Locate every Plasmodium parasite.
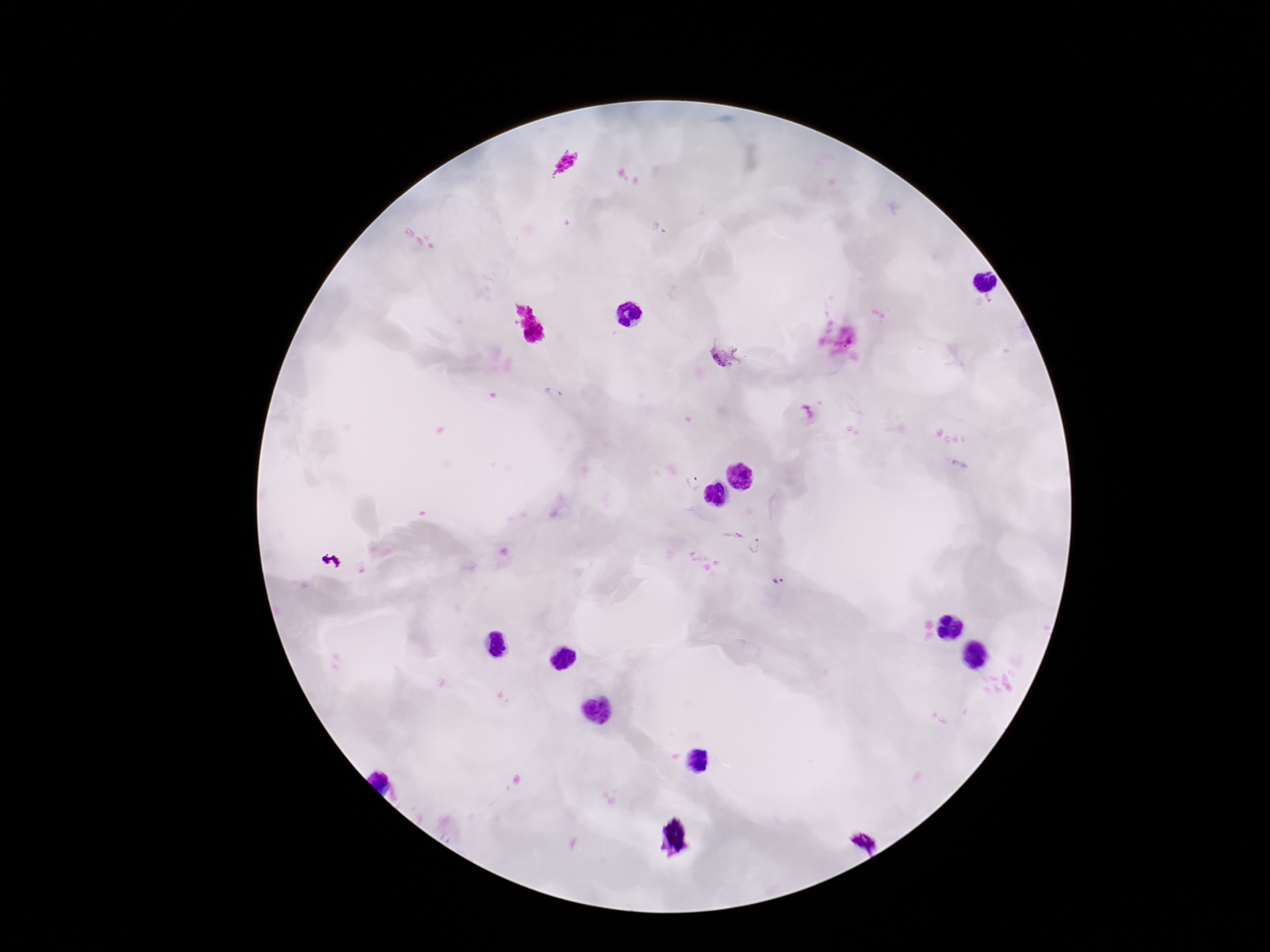
Approximate object centers, in pixels from the top-left corner.
Plasmodium parasites: (x=660, y=229), (x=724, y=356), (x=552, y=393), (x=693, y=482), (x=734, y=534), (x=757, y=547), (x=779, y=581).

Patient malaria status: positive. Image is 1270×952 pixels. One field from this slide. 100x magnification. Smartphone photograph taken through the microscope eyepiece. Giemsa-stained preparation. Thick blood film.